Point out each leukocyte.
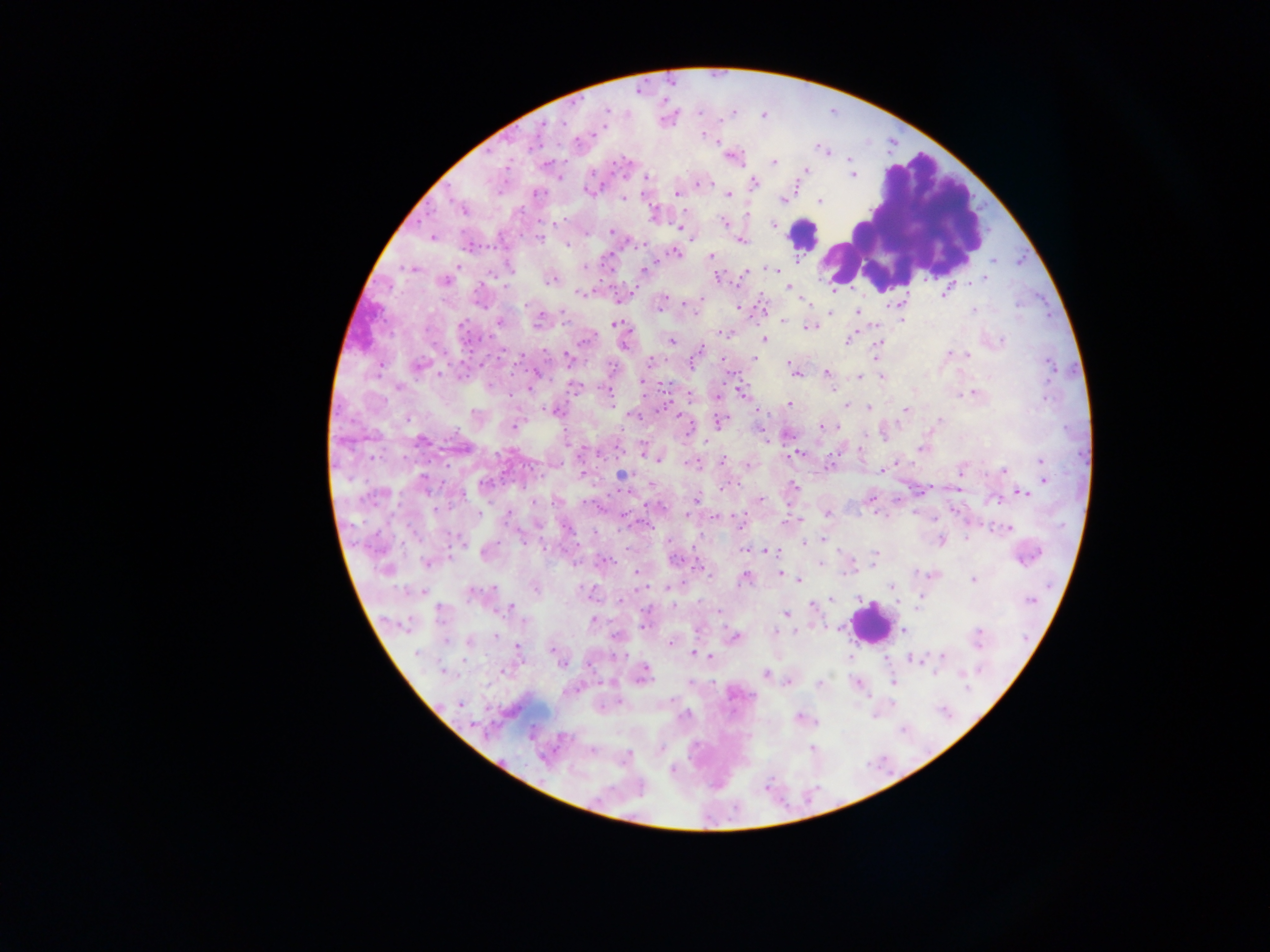
Approximate centers as x y in pixels.
Leukocytes: 902 221; 804 235; 869 623.

Plasmodium parasite locations: 608 110; 562 122; 542 126; 703 134; 532 145; 820 148; 824 150; 774 161; 807 169; 852 175; 647 177; 754 182; 699 184; 588 191; 538 193; 676 193; 728 195; 624 198; 782 201; 820 201; 462 210; 724 222; 773 225; 680 228; 611 231; 432 238; 540 239; 742 242; 568 244; 676 253; 710 256; 994 260; 459 266; 584 267; 408 268; 510 268; 644 269; 770 269; 745 273; 718 278; 984 278; 552 280; 978 280; 445 281; 506 287; 788 287; 580 292; 945 292; 664 298; 660 304; 689 304; 527 305; 739 308; 974 310; 857 312; 831 313; 902 319; 783 321; 499 323; 538 323; 616 325; 810 326; 462 328; 723 333; 586 339; 763 339; 848 340; 672 341; 1001 341; 878 343; 624 344; 701 349; 949 354; 966 355; 876 357; 520 358; 567 358; 754 358; 651 361; 419 365; 790 365; 1051 366; 611 367; 795 373; 826 373; 440 374; 860 377; 882 377; 642 382; 489 386; 574 387; 399 388; 741 392; 973 394; 690 396; 1046 397; 789 403; 845 406; 869 409; 906 409; 555 411; 634 415; 679 416; 408 418; 939 420; 719 422; 515 427; 821 427; 422 440; 920 448; 796 454; 658 460; 722 461; 1040 461; 691 463; 749 465; 882 470; 1003 470; 960 472; 582 473; 1043 473; 623 475; 423 476; 1045 481; 484 483; 651 483; 794 485; 725 487; 1022 493; 462 496; 871 497; 697 499; 761 500; 995 500; 436 508; 480 513; 687 514; 827 514; 508 515; 716 517; 797 521; 785 522; 568 529; 1009 529; 521 537; 967 538; 822 539; 940 540; 805 543; 744 548; 768 551; 484 554; 874 554; 605 561; 675 561; 873 561; 428 563; 820 564; 850 570; 637 574; 781 574; 744 579; 799 580; 973 580; 892 586; 534 587; 668 588; 472 594; 921 597; 622 599; 831 599; 1030 600; 673 605; 812 605; 511 608; 785 615; 593 620; 524 621; 904 630; 774 633; 978 635; 497 636; 735 637; 446 641; 469 642; 670 643; 519 648; 551 650; 416 653; 695 653; 943 656; 709 657; 912 659; 562 664; 645 670; 443 672; 935 673; 764 674; 965 674; 691 681; 788 682; 893 682; 819 683; 967 688; 671 699; 459 704; 686 715; 800 717; 811 749; 591 750; 628 755. Collected in Ghana. Thick blood film. One field of view. Image is 1270×952 pixels. Photographed through a microscope with a mobile-phone camera.